Assess the morphology of the red blood cells.
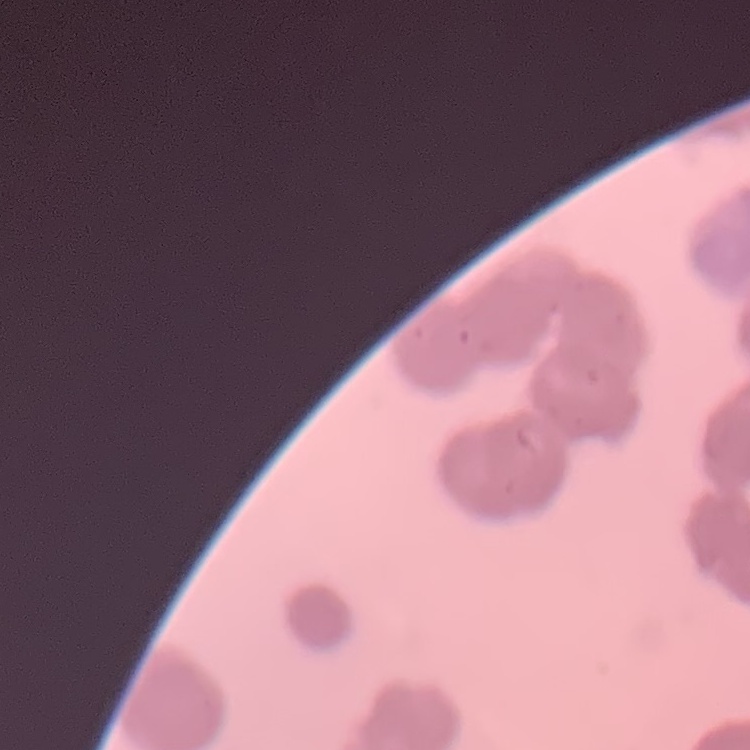

They show rouleaux formation.

stain = Field's or Giemsa
image type = one tile cut from a larger photomicrograph
preparation = thin peripheral smear